Point out each Plasmodium parasite.
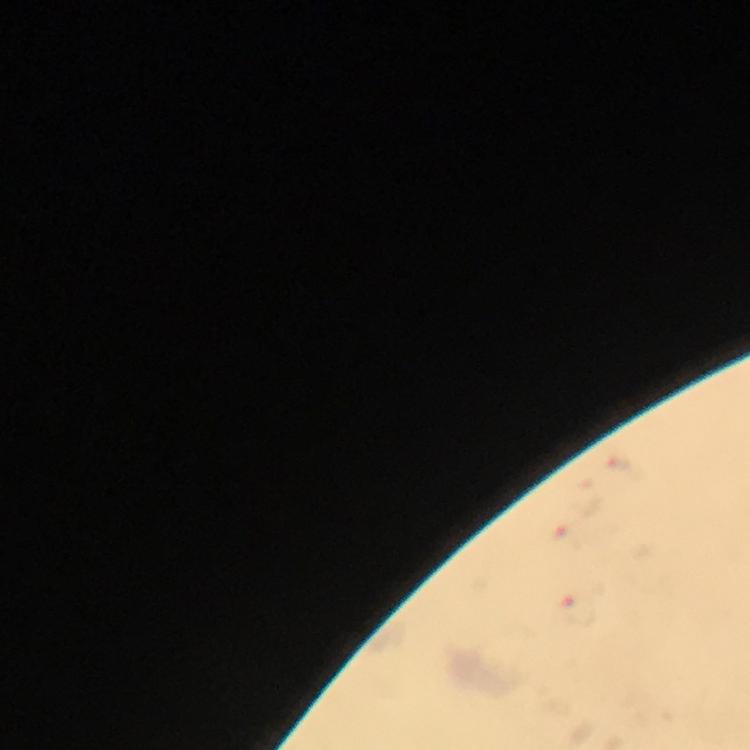

Approximate centers as (x, y) in pixels.
Plasmodium parasites: (622, 467), (572, 539), (578, 610).

From a diagnostic examination for malaria. Cropped region of a single field of view. Thick blood film. Giemsa stain. Photographed through the microscope with a smartphone camera. At 100x magnification. Image is 750×750 pixels. Immersion oil was used.